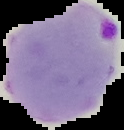
{
  "preparation": "thin blood film",
  "image_size": "124×130 pixels",
  "image_type": "cell region segmented out of the field of view; surrounding area masked to black",
  "result": "Plasmodium parasites identified"
}